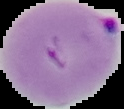
Summary:
  - Preparation: thin blood smear
  - Image size: 124×109 pixels
  - Malaria status: parasitized
  - Image type: cell region segmented out of the field of view; surrounding area masked to black